Report the malaria status of this cell.
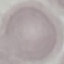

Uninfected.

Summary:
  - Capture: smartphone through the microscope eyepiece
  - Image type: cell patch, automatically extracted from a larger field of view and resized to 64 × 64 pixels
  - Preparation: thin smear
  - Stain: Giemsa